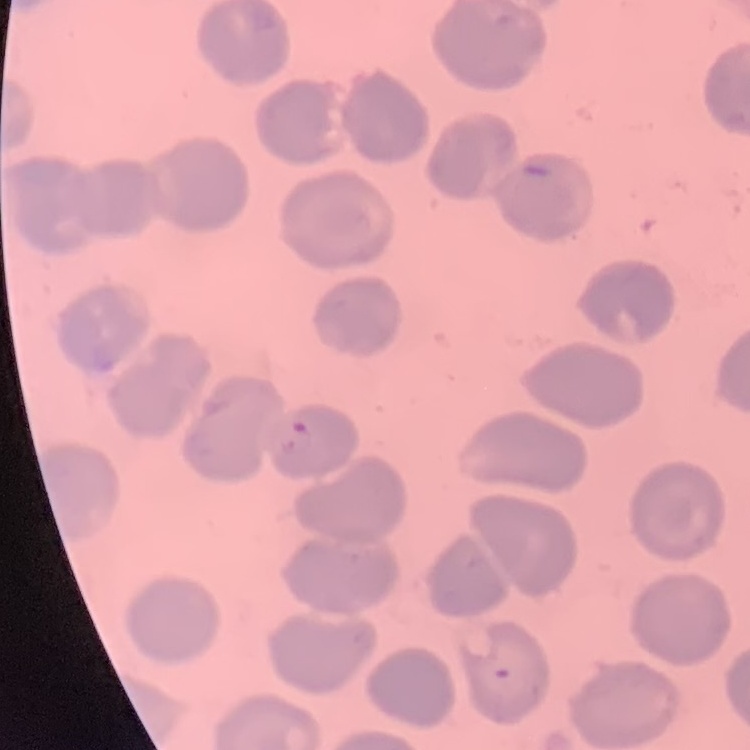
red blood cell morphology = no rouleaux formation
preparation = thin blood film
image type = square crop of a larger photomicrograph
stain = Field's or Giemsa